Outline every leukocyte.
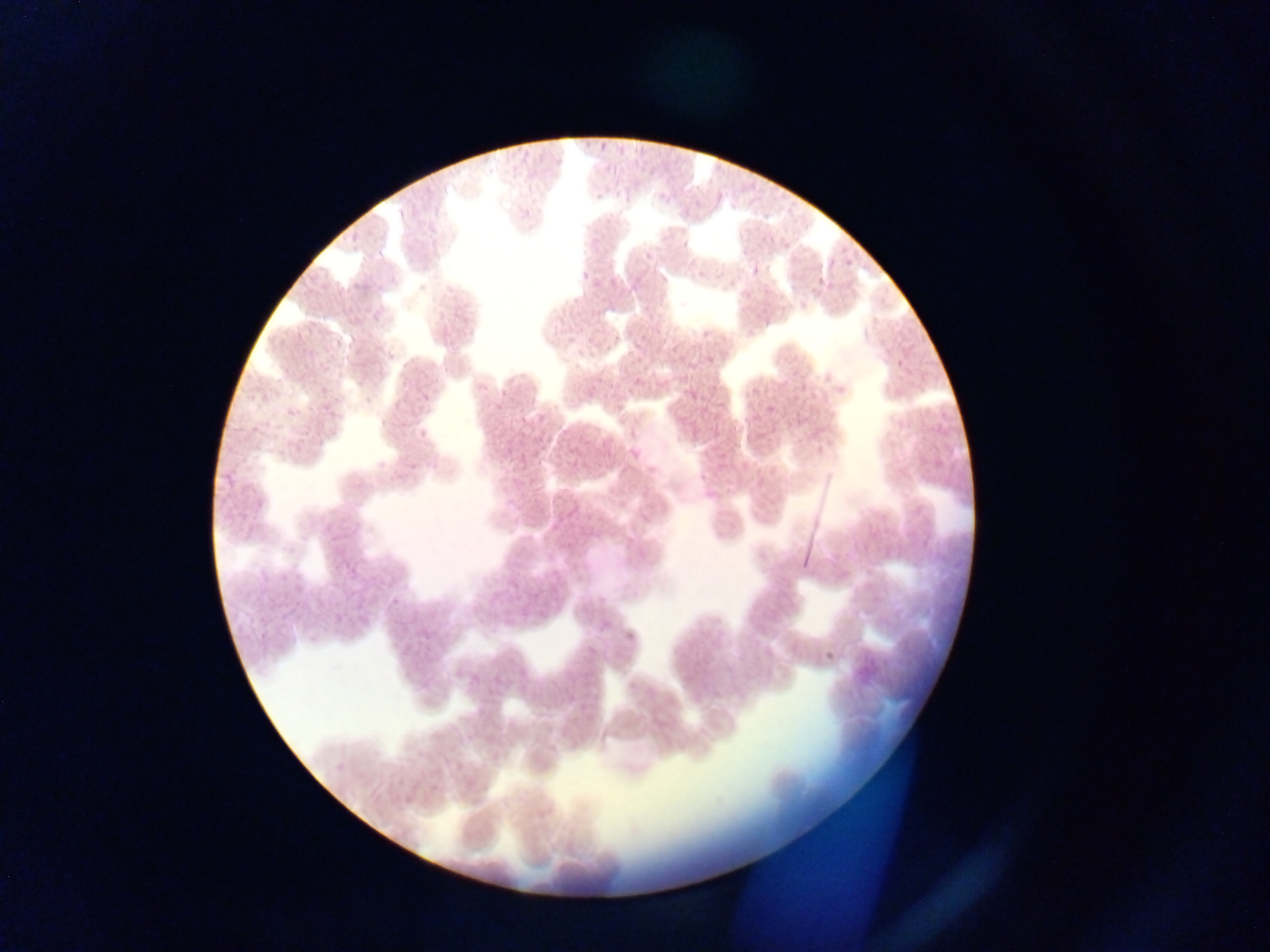

No leukocytes observed.

{
  "preparation": "thin blood smear",
  "image_size": "1270×952 pixels",
  "plasmodium_parasite_locations": "approximate bounding boxes as {left, top, right, bottom} in pixels: {576, 269, 591, 280}, {417, 276, 433, 295}, {832, 377, 850, 395}, {763, 396, 777, 417}, {415, 423, 431, 438}, {408, 463, 418, 472}, {695, 470, 711, 484}, {254, 502, 269, 512}, {391, 590, 404, 606}, {622, 630, 631, 644}, {822, 648, 837, 663}, {333, 761, 345, 773}",
  "country": "Ghana",
  "capture": "mobile-phone photograph through a microscope",
  "field_of_view": "single"
}